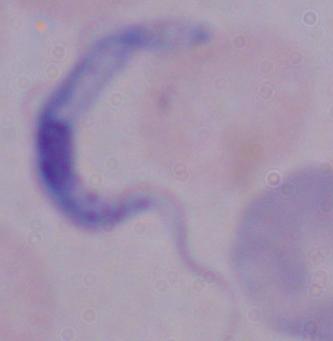
Captured at 1000x magnification. Photomicrograph. A trypanosome is shown.